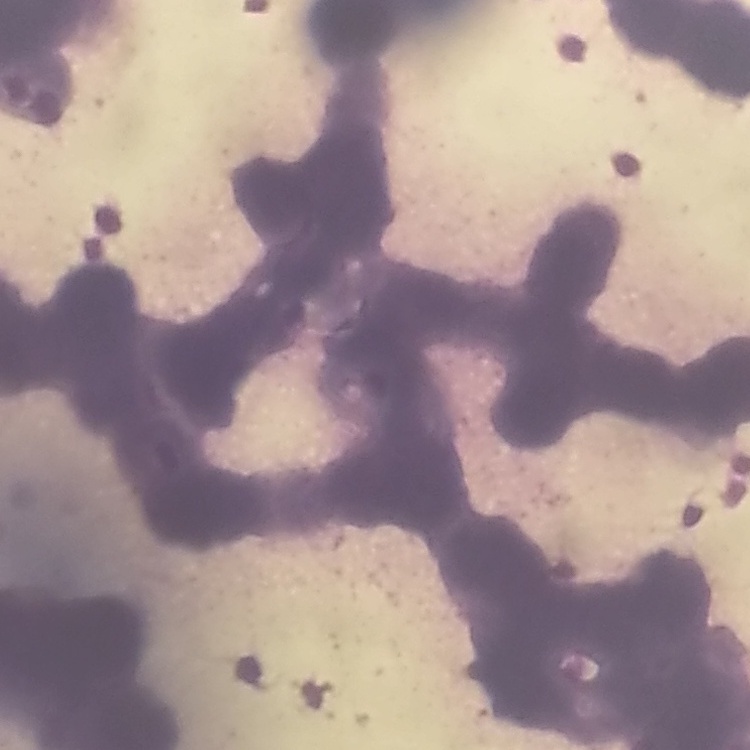

Summary:
  - Erythrocyte morphology: rouleaux formation
  - Stain: Field's or Giemsa
  - Preparation: thin blood film
  - Image type: square crop of a larger photomicrograph